Point out each Plasmodium parasite.
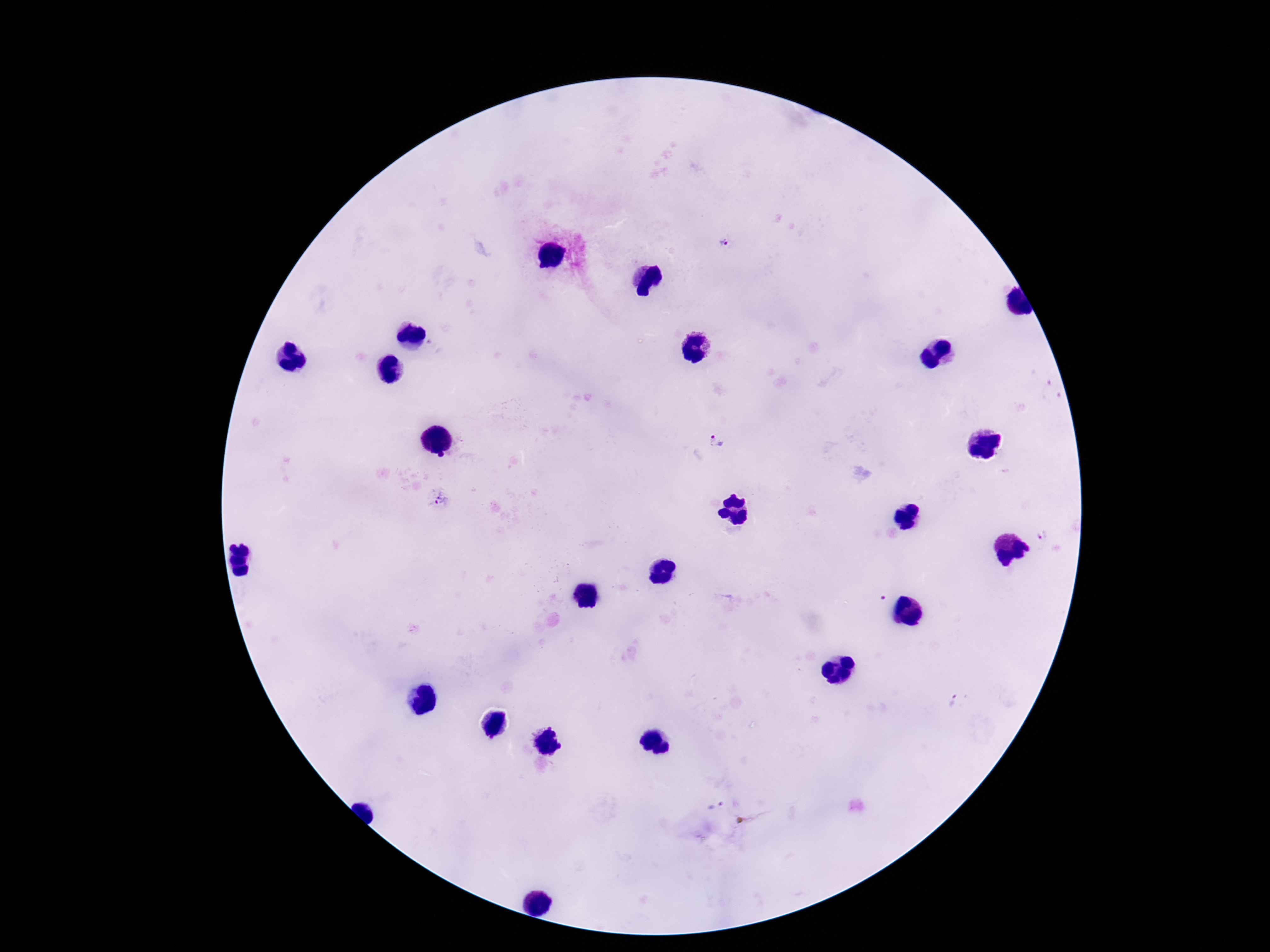
Approximate centers as (x, y) in pixels.
Plasmodium parasites: (727, 241), (716, 445), (440, 501), (1043, 536), (953, 700), (715, 802).

Summary:
  - Image size: 1270×952 pixels
  - Magnification: 100x
  - Stain: Giemsa
  - Field of view: one from this slide
  - Patient malaria status: positive
  - Preparation: thick peripheral-blood smear
  - Capture: smartphone camera through the microscope eyepiece